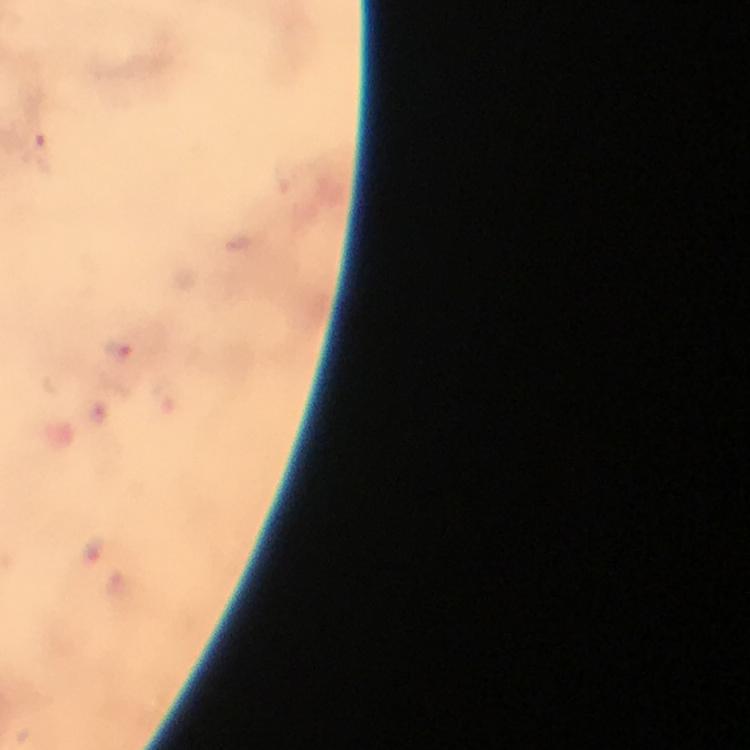

Approximate centers as (x, y) in pixels.
Summary:
  - Malaria parasite locations: (39, 146), (117, 348)
  - Stain: Giemsa
  - Capture: smartphone camera through the microscope
  - Cropped from: a single field of view
  - Context: from a diagnostic examination for malaria
  - Immersion oil: used
  - Magnification: 100x
  - Image size: 750×750 pixels
  - Preparation: thick smear